State the preparation type.
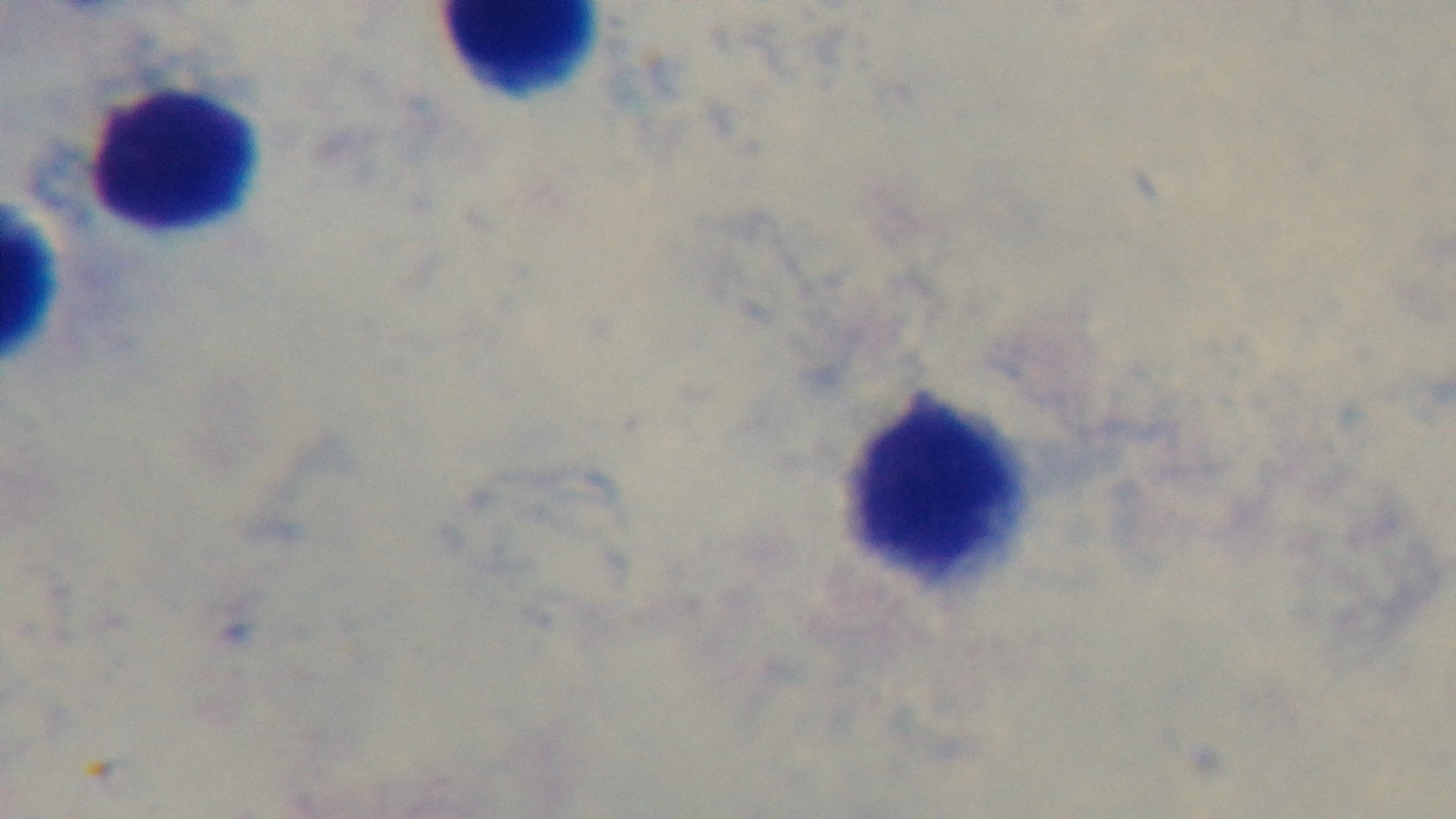

Thick.

Giemsa stain. One field from the slide. Mounted 4K digital camera. Photomicrograph. Oil-immersion objective, 100x. Malaria status: negative.